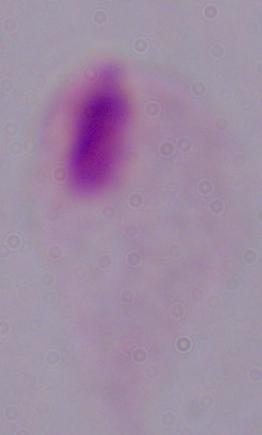
Summary:
  - Magnification: 1000x
  - Identification: trichomonad
  - Modality: micrograph